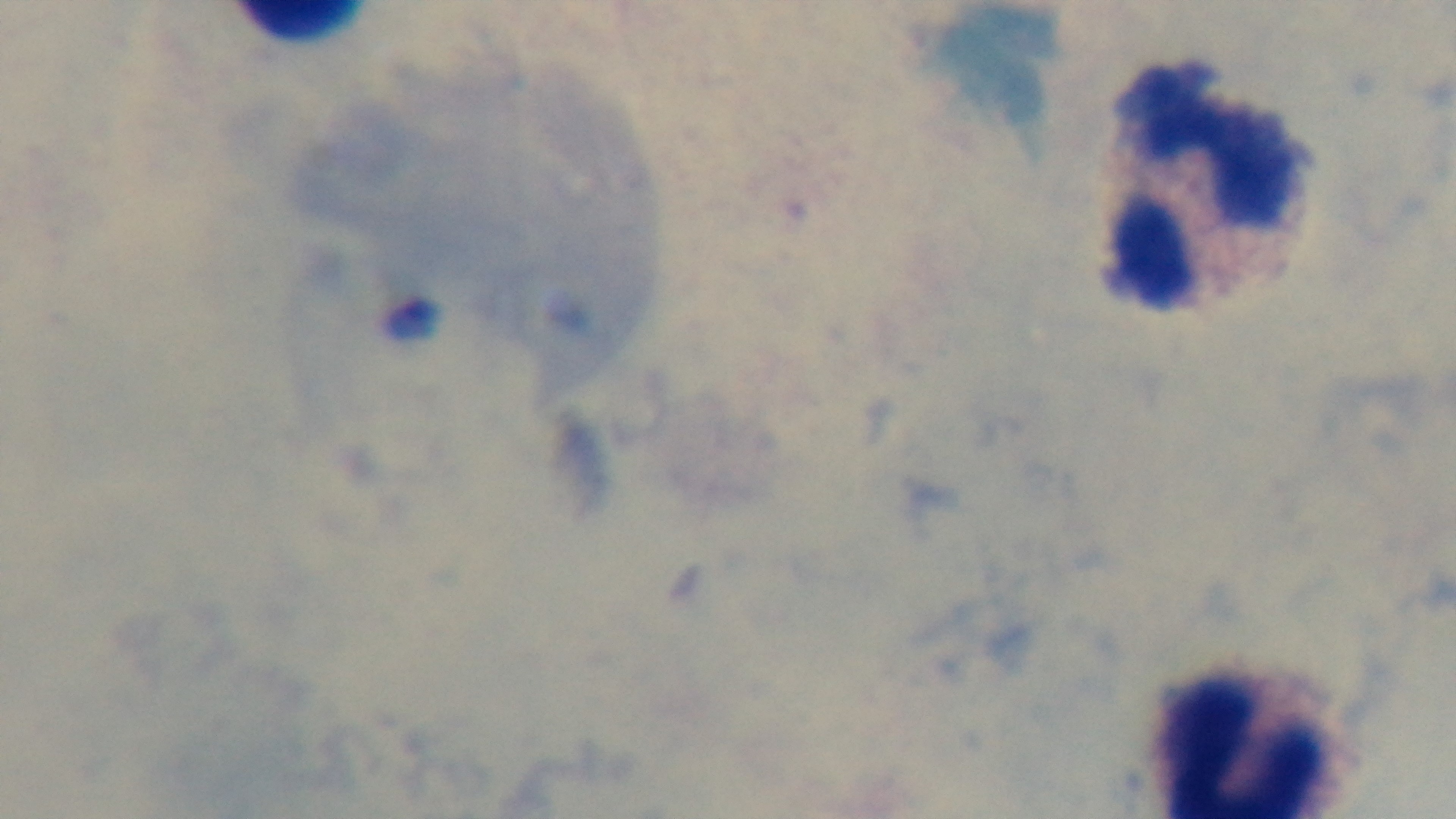
Photomicrograph. Preparation: thick. Malaria status: negative. Single field of view. Oil-immersion objective, 100x. Mounted 4K digital camera. Giemsa stain.